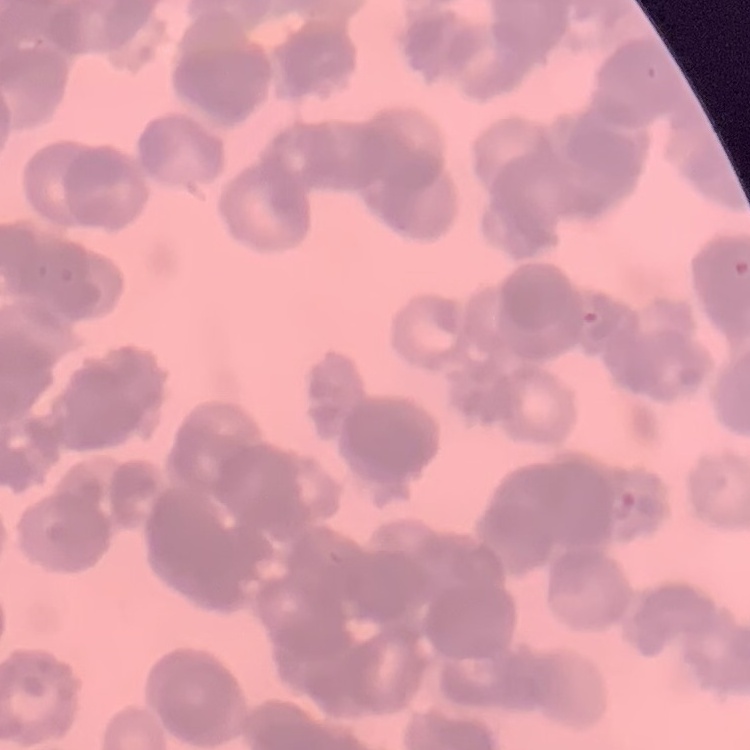
Summary:
  - Erythrocyte morphology: rouleaux formation
  - Stain: Field's or Giemsa
  - Image type: square crop of a larger photomicrograph
  - Preparation: thin blood smear